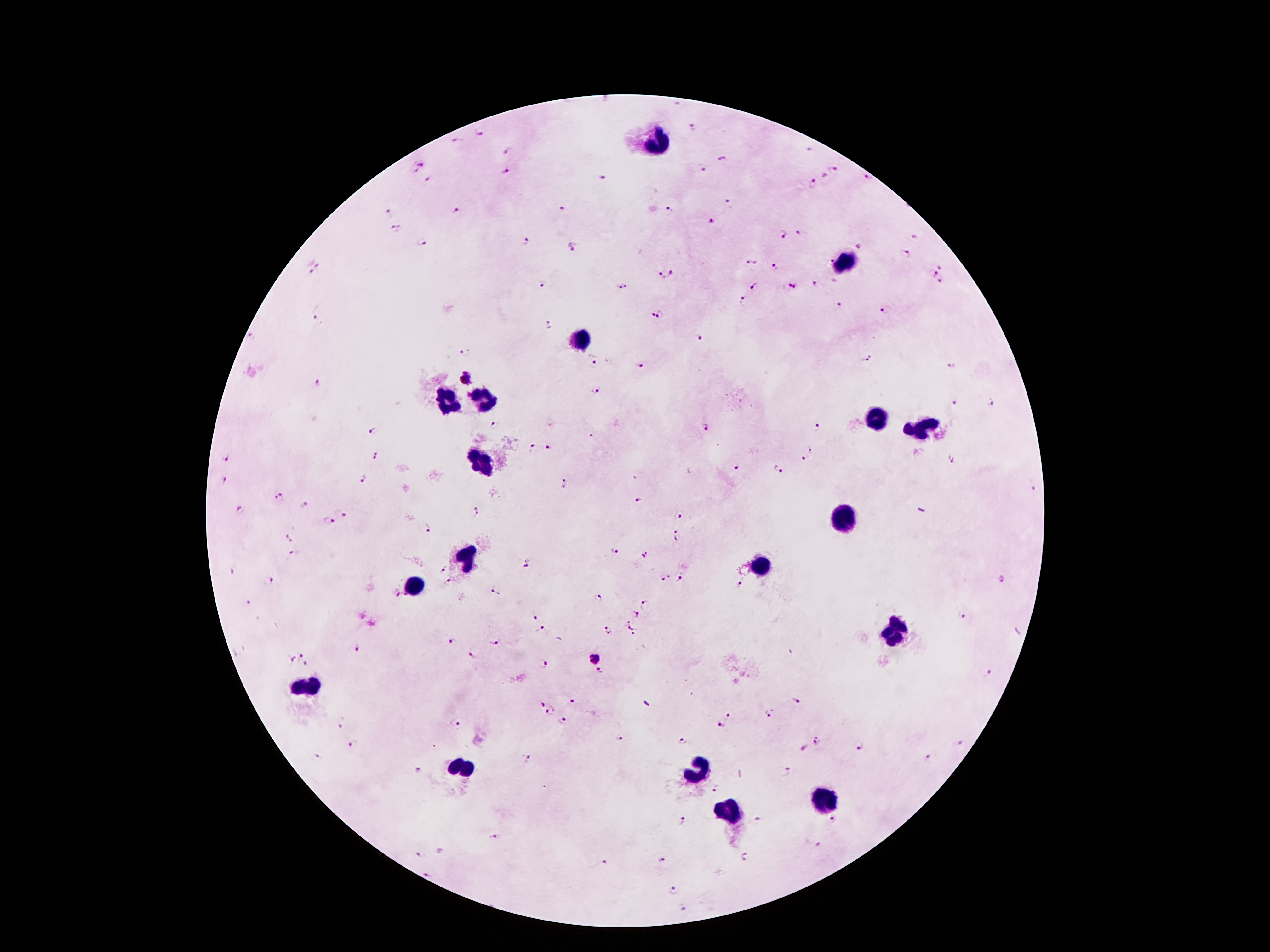
Approximate centers as [x, y] in pixels.
Summary:
  - Plasmodium parasite locations: [693, 128], [480, 133], [457, 141], [809, 150], [509, 151], [723, 160], [417, 165], [703, 169], [506, 170], [835, 170], [825, 177], [869, 177], [602, 179], [428, 181], [810, 184], [731, 202], [562, 209], [456, 211], [668, 211], [388, 213], [712, 222], [397, 228], [801, 232], [782, 234], [915, 237], [524, 243], [422, 244], [574, 247], [860, 248], [906, 253], [752, 262], [829, 262], [776, 265], [941, 266], [313, 267], [673, 273], [934, 273], [663, 275], [940, 283], [815, 284], [754, 285], [543, 286], [623, 287], [792, 287], [744, 298], [839, 305], [886, 310], [652, 315], [660, 315], [316, 320], [549, 324], [252, 336], [700, 338], [465, 351], [593, 357], [866, 357], [639, 365], [952, 366], [467, 378], [316, 383], [596, 388], [956, 402], [993, 402], [494, 424], [818, 425], [709, 427], [374, 429], [549, 448], [534, 449], [812, 449], [376, 456], [227, 457], [950, 458], [802, 459], [736, 468], [778, 469], [224, 480], [362, 481], [565, 484], [1033, 488], [280, 498], [638, 501], [303, 506], [477, 510], [341, 511], [241, 512], [678, 515], [327, 523], [427, 530], [677, 530], [291, 536], [677, 540], [615, 550], [294, 554], [645, 554], [528, 565], [234, 570], [443, 570], [671, 574], [682, 578], [1005, 578], [662, 579], [271, 581], [449, 582], [742, 584], [494, 592], [395, 595], [597, 598], [249, 601], [646, 604], [637, 614], [963, 615], [535, 618], [628, 621], [633, 627], [542, 630], [608, 630], [634, 635], [453, 640], [493, 641], [359, 648], [302, 653], [472, 655], [594, 657], [289, 660], [306, 665], [541, 665], [603, 670], [990, 673], [571, 700], [799, 701], [541, 704], [551, 712], [768, 714], [728, 715], [564, 721], [342, 722], [455, 722], [720, 726], [619, 738], [684, 740], [816, 741], [959, 743], [861, 745], [353, 746], [319, 758], [527, 758], [927, 758], [420, 770], [788, 772], [714, 791], [758, 819], [682, 820], [835, 820], [493, 837], [819, 845], [420, 854], [745, 856], [663, 859], [604, 862], [429, 877], [676, 890], [683, 909]
  - Leukocyte locations: [656, 143], [843, 263], [578, 339], [485, 399], [444, 404], [872, 415], [922, 426], [480, 461], [848, 515], [465, 558], [763, 568], [417, 585], [893, 633], [309, 686], [459, 769], [698, 770], [826, 798], [729, 813]
  - Capture: smartphone through the microscope eyepiece
  - Patient malaria status: infected with Plasmodium falciparum
  - Image size: 1270×952 pixels
  - Field of view: single
  - Magnification: 100x
  - Stain: Giemsa
  - Preparation: thick peripheral-blood smear